Report the malaria status of this cell.
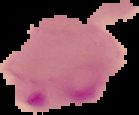

It is parasitized.

From a thin blood smear. Image is 139×115 pixels. Cell region segmented out of the field of view; the surrounding area is masked to black.